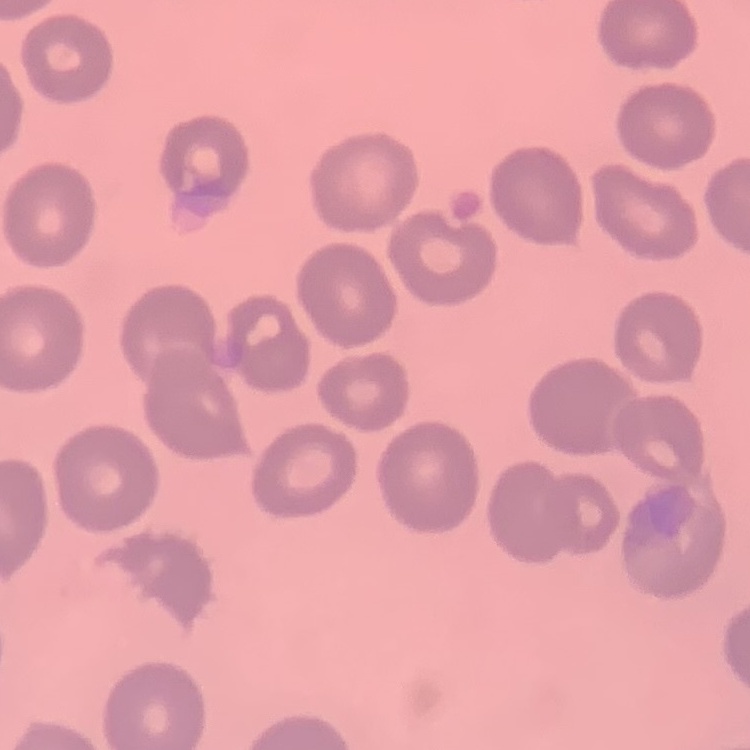

red blood cell morphology = no rouleaux formation
image type = one tile cut from a larger photomicrograph
preparation = thin peripheral smear
stain = Field's or Giemsa